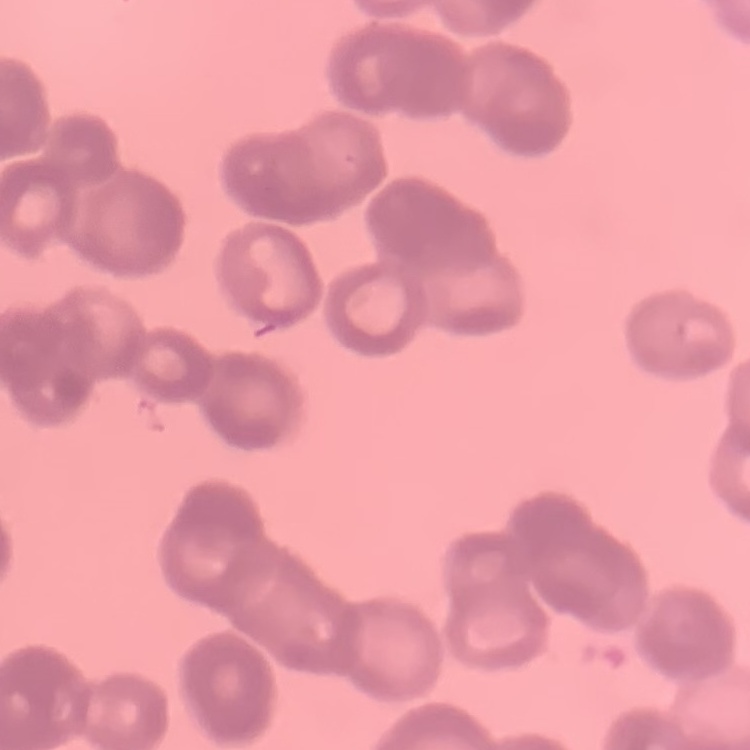

{
  "red_blood_cell_morphology": "rouleaux formation",
  "preparation": "thin blood film",
  "image_type": "one tile cut from a larger photomicrograph",
  "stain": "Field's or Giemsa"
}